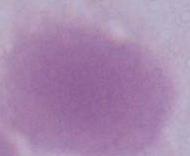
Photomicrograph. Captured at 1000x magnification. An erythrocyte is seen.